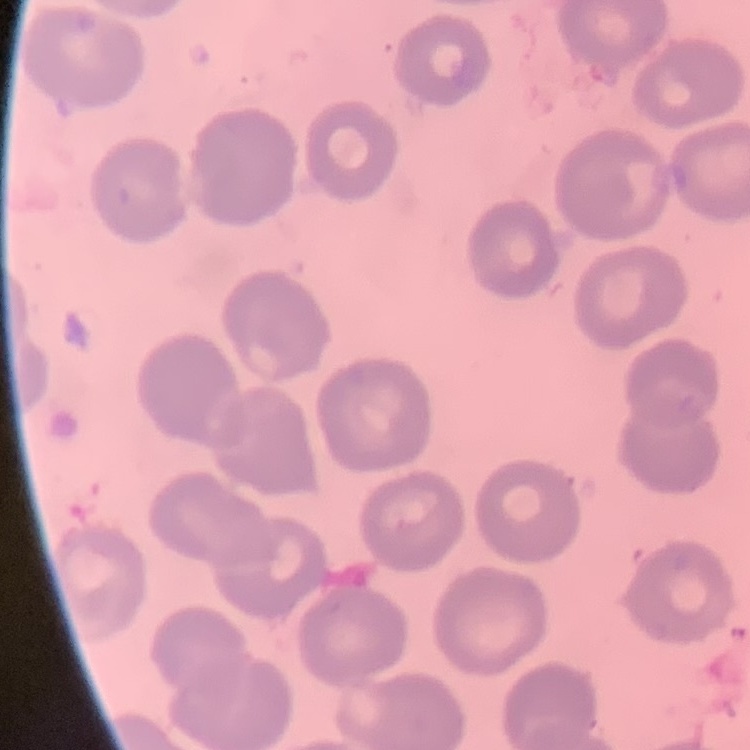 The red blood cells show no rouleaux formation. Thin blood smear. Stained with either Field's or Giemsa. Square crop of a larger photomicrograph.